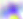

400x magnification. Toxoplasma gondii is shown. Photomicrograph.